Outline each Plasmodium falciparum-infected red blood cell.
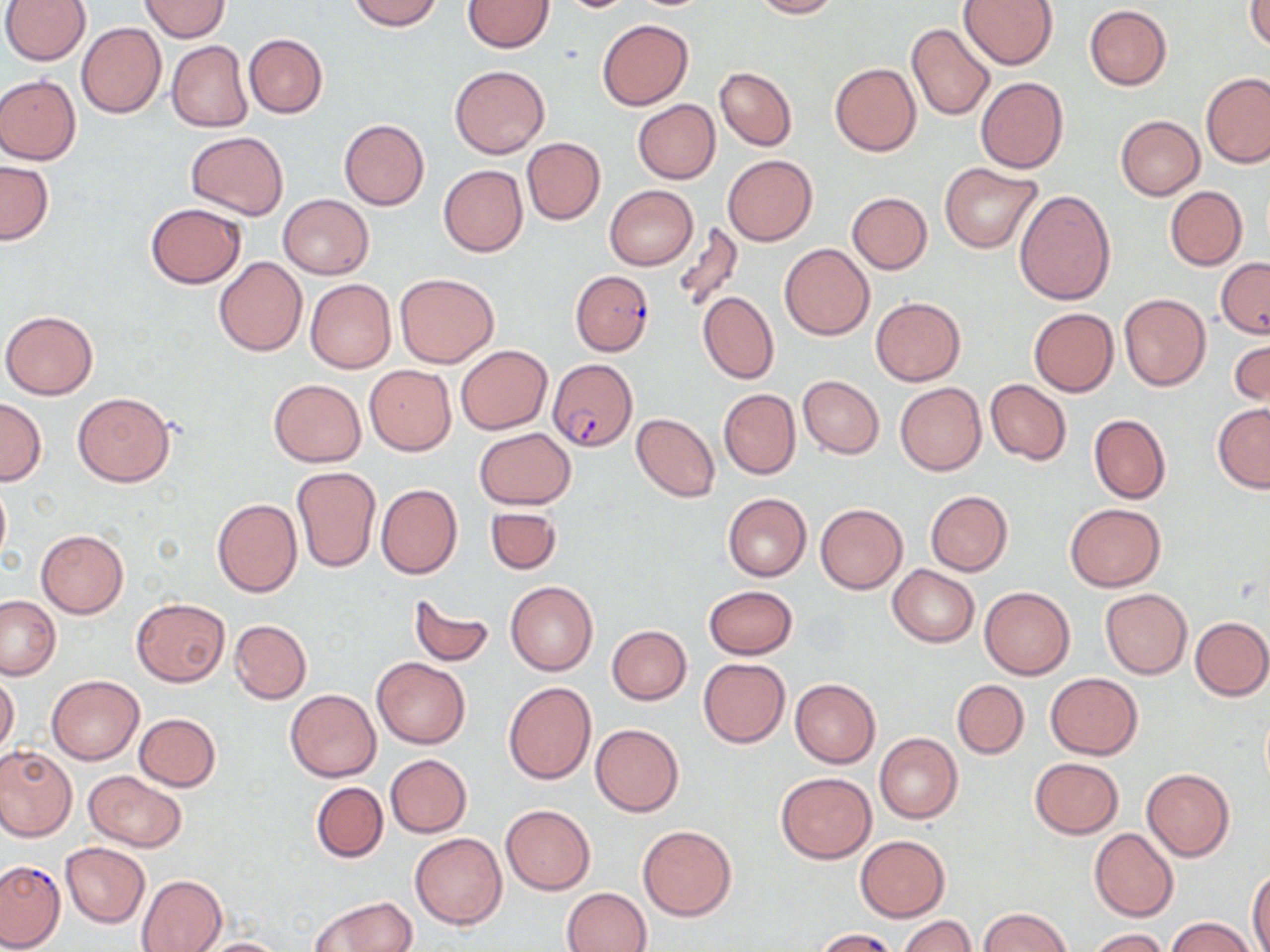

Approximate bounding boxes as [x1, y1, x2, y2] in pixels.
Plasmodium falciparum-infected red blood cells: [569, 272, 652, 356], [549, 358, 637, 452].

slide-level diagnosis = Plasmodium falciparum
magnification = 1000x
modality = optical microscopy
preparation = thin blood film
field of view = single
image size = 1270×952 pixels
uninfected red blood cell locations = approximate bounding boxes as [x1, y1, x2, y2] in pixels: [2, 0, 90, 64], [142, 0, 230, 41], [349, 0, 443, 30], [556, 0, 641, 14], [751, 0, 840, 18], [958, 0, 1059, 70], [463, 1, 553, 52], [1247, 2, 1270, 51], [1084, 4, 1171, 90], [597, 19, 693, 110], [76, 21, 167, 118], [906, 22, 995, 121], [244, 33, 328, 119], [168, 41, 253, 132], [830, 63, 921, 156], [450, 65, 550, 159], [714, 66, 796, 151], [1201, 72, 1269, 168], [0, 75, 81, 165], [975, 77, 1068, 173], [632, 100, 719, 183], [1116, 115, 1204, 200], [339, 119, 429, 210], [187, 131, 288, 219], [522, 137, 605, 225], [722, 154, 817, 247], [0, 160, 54, 245], [939, 163, 1043, 253], [438, 165, 527, 256], [604, 184, 699, 270], [1164, 185, 1248, 271], [1014, 188, 1116, 306], [847, 192, 932, 273], [277, 194, 373, 279], [145, 203, 246, 288], [671, 222, 744, 315], [781, 243, 875, 340], [1217, 256, 1270, 338], [214, 257, 307, 356], [395, 272, 498, 367], [307, 279, 396, 373], [698, 292, 778, 383], [1119, 294, 1210, 392], [869, 297, 966, 385], [1028, 308, 1119, 397], [2, 310, 98, 400], [1229, 331, 1268, 410], [455, 344, 552, 435], [363, 364, 456, 455], [798, 375, 884, 458], [268, 379, 366, 467], [985, 379, 1072, 465], [895, 382, 986, 475], [718, 388, 799, 480], [72, 392, 175, 486], [0, 397, 46, 484], [1212, 402, 1270, 492], [632, 413, 719, 502], [1089, 414, 1170, 504], [473, 428, 577, 509], [290, 466, 381, 572], [0, 479, 10, 569], [375, 483, 462, 579], [925, 491, 1013, 576], [722, 492, 811, 581], [212, 498, 302, 598], [1065, 502, 1166, 592], [815, 503, 907, 594], [485, 506, 562, 573], [36, 529, 128, 617], [888, 564, 979, 646], [506, 582, 597, 676], [702, 585, 797, 659], [979, 586, 1075, 678], [1100, 588, 1192, 678], [409, 592, 495, 668], [0, 597, 61, 680], [132, 598, 230, 686], [1190, 615, 1270, 700], [230, 620, 311, 704], [607, 625, 691, 704], [371, 656, 471, 749], [699, 657, 789, 747], [0, 672, 19, 757], [1046, 672, 1142, 759], [46, 675, 143, 764], [789, 679, 880, 768], [952, 679, 1028, 758], [502, 682, 597, 786], [285, 688, 381, 781], [134, 713, 221, 791], [591, 724, 684, 817], [875, 732, 962, 823], [0, 745, 76, 841], [385, 753, 471, 836], [1030, 757, 1124, 838], [1142, 768, 1234, 861], [82, 771, 187, 851], [775, 772, 876, 864], [311, 782, 388, 863], [501, 805, 594, 895], [638, 825, 735, 922], [1089, 828, 1179, 923], [410, 833, 506, 930], [854, 835, 950, 921], [61, 843, 149, 927], [1248, 868, 1270, 952], [137, 874, 227, 952], [562, 887, 651, 952], [311, 895, 413, 951], [978, 907, 1070, 952], [897, 915, 976, 952], [1167, 917, 1256, 952], [811, 928, 898, 951], [1088, 928, 1169, 952], [194, 938, 292, 952]
stain = May-Grünwald-Giemsa